Identify the parasite.
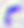

Toxoplasma gondii.

Summary:
  - Modality: micrograph
  - Magnification: 400x